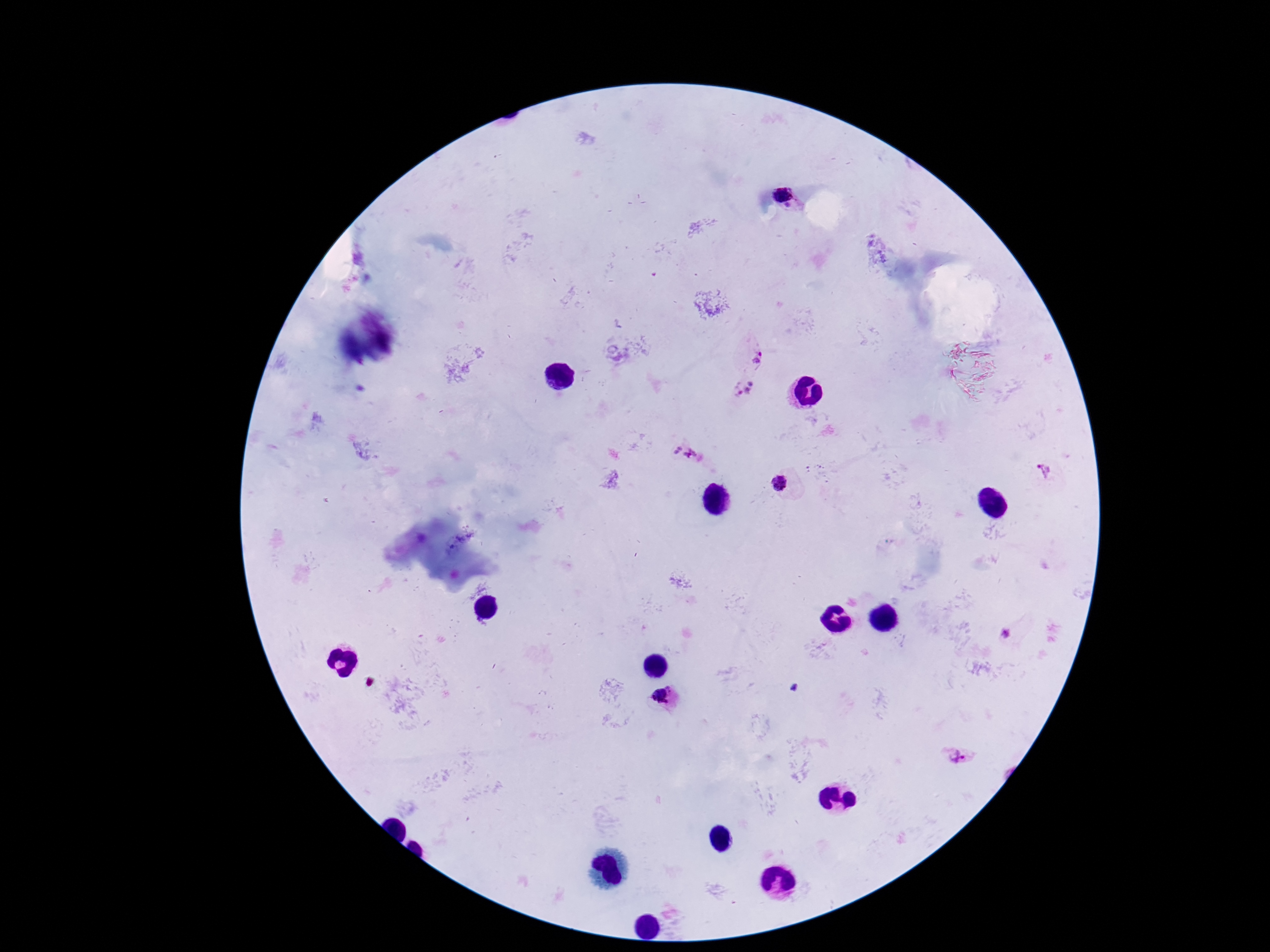
patient malaria status = positive
magnification = 100x
capture = smartphone camera through the microscope eyepiece
image size = 1270×952 pixels
Plasmodium parasite locations = approximate centers as [x, y] in pixels: [786, 194], [757, 358], [743, 388], [685, 453], [1045, 473], [781, 484], [1006, 633], [662, 695], [959, 755]
stain = Giemsa
preparation = thick blood smear
field of view = single